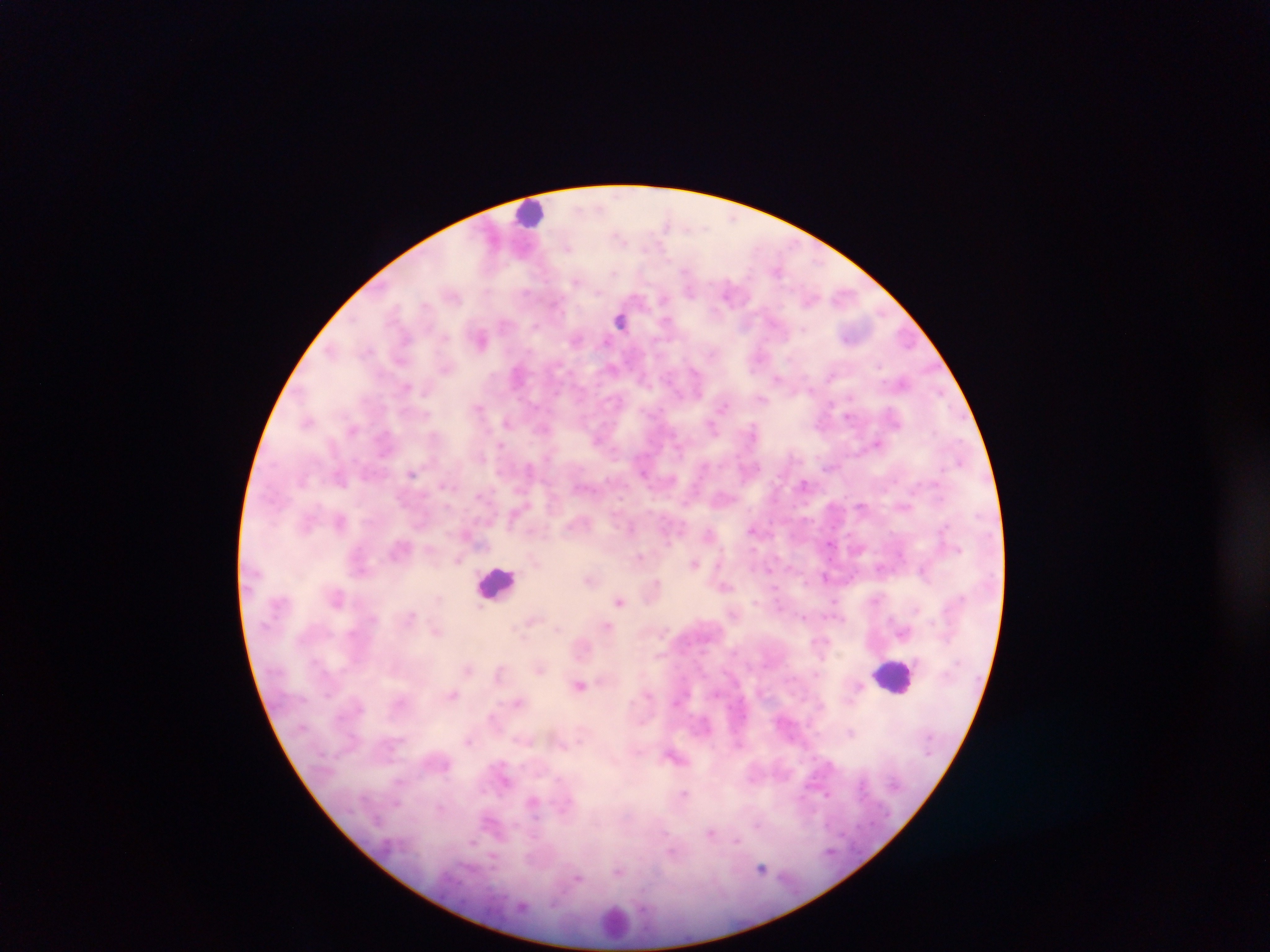
Approximate centers as [x, y] in pixels. Leukocyte locations: [532, 213], [498, 584], [895, 676], [616, 922]. Plasmodium parasite locations: [666, 223], [620, 236], [567, 247], [777, 271], [576, 282], [690, 290], [728, 292], [664, 299], [425, 305], [620, 320], [666, 321], [504, 323], [745, 324], [535, 328], [803, 329], [445, 336], [405, 339], [577, 339], [481, 340], [331, 350], [712, 352], [880, 366], [446, 369], [695, 372], [517, 375], [832, 375], [778, 378], [406, 386], [850, 398], [762, 399], [722, 406], [478, 408], [848, 416], [308, 422], [506, 422], [713, 428], [543, 429], [752, 429], [434, 435], [878, 443], [501, 445], [960, 461], [704, 464], [529, 468], [412, 473], [642, 473], [339, 479], [804, 483], [443, 486], [593, 491], [861, 506], [340, 522], [630, 527], [753, 529], [708, 534], [829, 544], [641, 557], [457, 560], [695, 563], [880, 568], [922, 570], [825, 577], [588, 581], [657, 581], [725, 586], [619, 600], [876, 600], [833, 602], [755, 603], [917, 609], [412, 615], [803, 617], [531, 621], [527, 625], [607, 626], [557, 629], [436, 632], [518, 633], [468, 668], [539, 670], [499, 671], [816, 674], [580, 685], [453, 694], [518, 702], [850, 732], [469, 741], [673, 756], [684, 793], [396, 803], [440, 808], [758, 825], [711, 832], [736, 841], [473, 842], [494, 856], [761, 868], [619, 871], [578, 879]. Thick blood film. Single field of view. Collected in Ghana. Image is 1270×952 pixels. Photographed through a microscope with a mobile-phone camera.